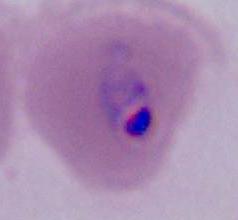
Captured at either 400x or 1000x magnification. A Plasmodium parasite is seen. Micrograph.